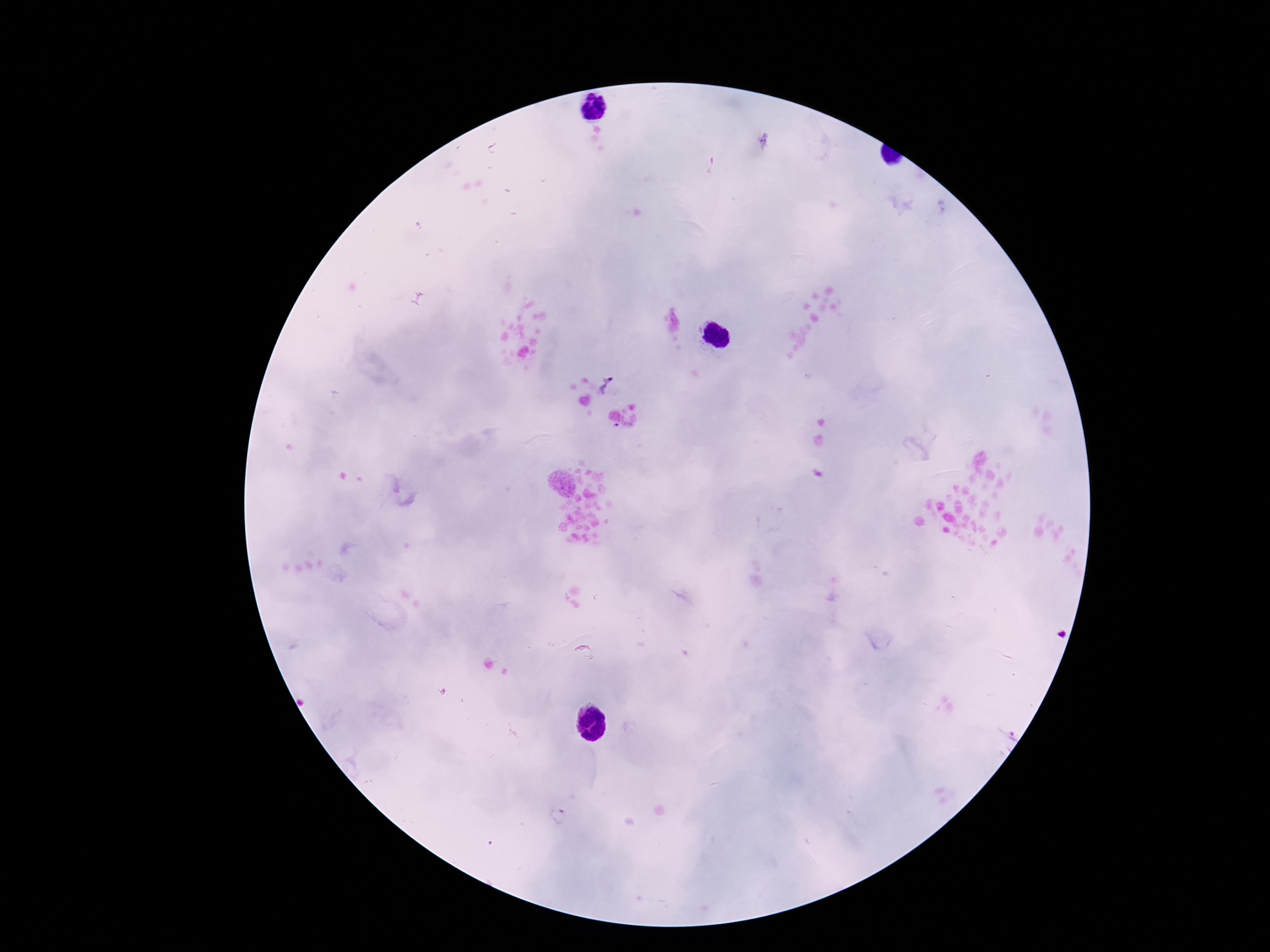

Approximate centers as [x, y] in pixels.
Summary:
  - Plasmodium parasite locations: [608, 386]
  - Patient malaria status: positive
  - Field of view: one from this slide
  - Preparation: thick blood film
  - Image size: 1270×952 pixels
  - Stain: Giemsa
  - Magnification: 100x
  - Capture: smartphone camera through the microscope eyepiece